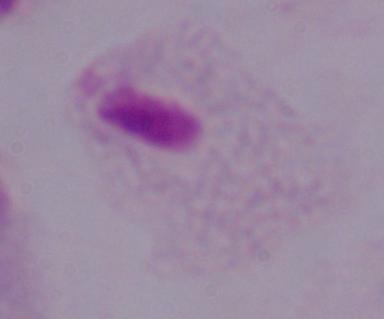
modality: photomicrograph
magnification: 1000x
identification: trichomonad